Report the malaria status of this cell.
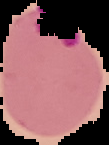
It is parasitized.

Image is 109×145 pixels. From a thin blood film. Cell region segmented out of the field of view; the surrounding area is masked to black.